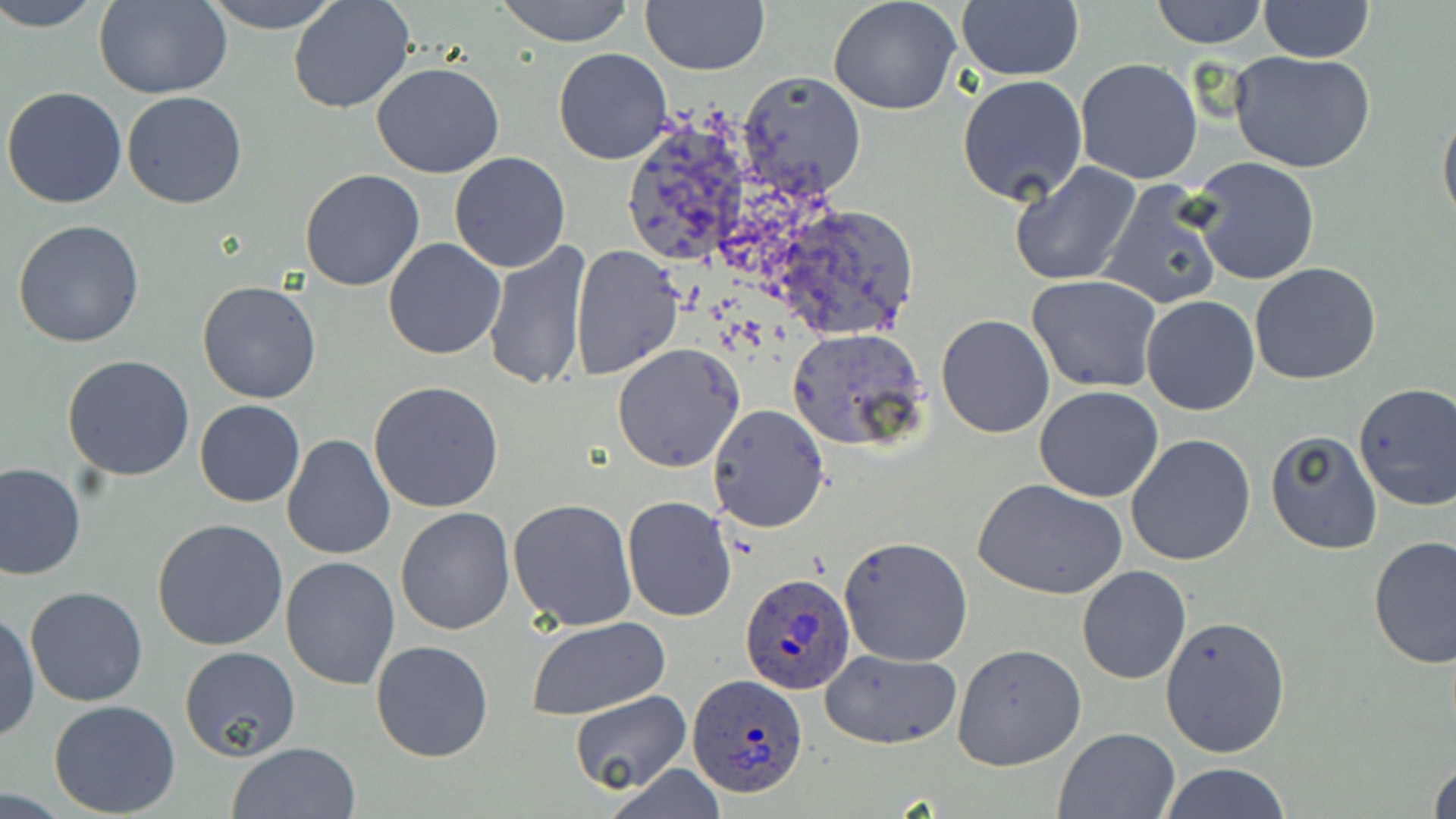
Summary:
  - Coordinate format: approximate bounding boxes as (x1, y1, x2, y2) in pixels
  - Uninfected red blood cell locations: (2, 0, 102, 31), (203, 0, 343, 33), (288, 0, 415, 115), (496, 0, 634, 46), (828, 0, 962, 115), (955, 0, 1084, 83), (1151, 0, 1267, 48), (96, 1, 231, 99), (641, 1, 768, 75), (1262, 1, 1374, 63), (553, 47, 673, 164), (1228, 51, 1377, 174), (1075, 58, 1203, 185), (372, 61, 504, 178), (737, 71, 867, 198), (957, 74, 1089, 206), (2, 85, 127, 208), (121, 91, 248, 210), (1438, 103, 1456, 234), (619, 113, 759, 273), (448, 152, 572, 273), (1191, 156, 1322, 287), (1008, 163, 1143, 287), (298, 168, 425, 292), (1096, 180, 1225, 312), (772, 204, 921, 341), (12, 220, 145, 350), (383, 239, 506, 359), (483, 241, 592, 393), (570, 247, 683, 379), (1249, 263, 1382, 385), (1027, 273, 1163, 392), (197, 279, 323, 403), (1141, 295, 1261, 416), (935, 314, 1056, 439), (786, 326, 928, 453), (612, 344, 746, 472), (63, 353, 196, 481), (369, 381, 504, 513), (1353, 383, 1456, 511), (1034, 385, 1164, 502), (194, 400, 305, 507), (708, 404, 831, 535), (1264, 429, 1382, 555), (1126, 433, 1257, 566), (281, 435, 396, 558), (0, 463, 85, 582), (972, 478, 1126, 603), (622, 496, 736, 622), (508, 497, 637, 630), (395, 507, 515, 636), (152, 518, 289, 652), (838, 536, 973, 667), (1367, 536, 1455, 668), (281, 556, 400, 690), (1077, 566, 1192, 683), (24, 586, 149, 707), (1, 611, 39, 743), (1159, 614, 1290, 758), (526, 616, 672, 722), (369, 640, 493, 763), (953, 644, 1087, 771), (179, 646, 302, 761), (818, 649, 963, 749), (570, 691, 689, 795), (48, 700, 182, 818), (1053, 728, 1179, 818), (227, 741, 363, 819), (1428, 754, 1456, 819), (1158, 763, 1292, 819), (600, 764, 729, 818)
  - Plasmodium ovale-infected red blood cell locations: (738, 573, 856, 696), (686, 673, 810, 801)
  - Slide-level diagnosis: Plasmodium ovale
  - Image size: 1456×819 pixels
  - Magnification: 1000x
  - Preparation: thin blood film
  - Stain: May-Grünwald-Giemsa
  - Modality: optical microscopy
  - Field of view: one of a larger specimen